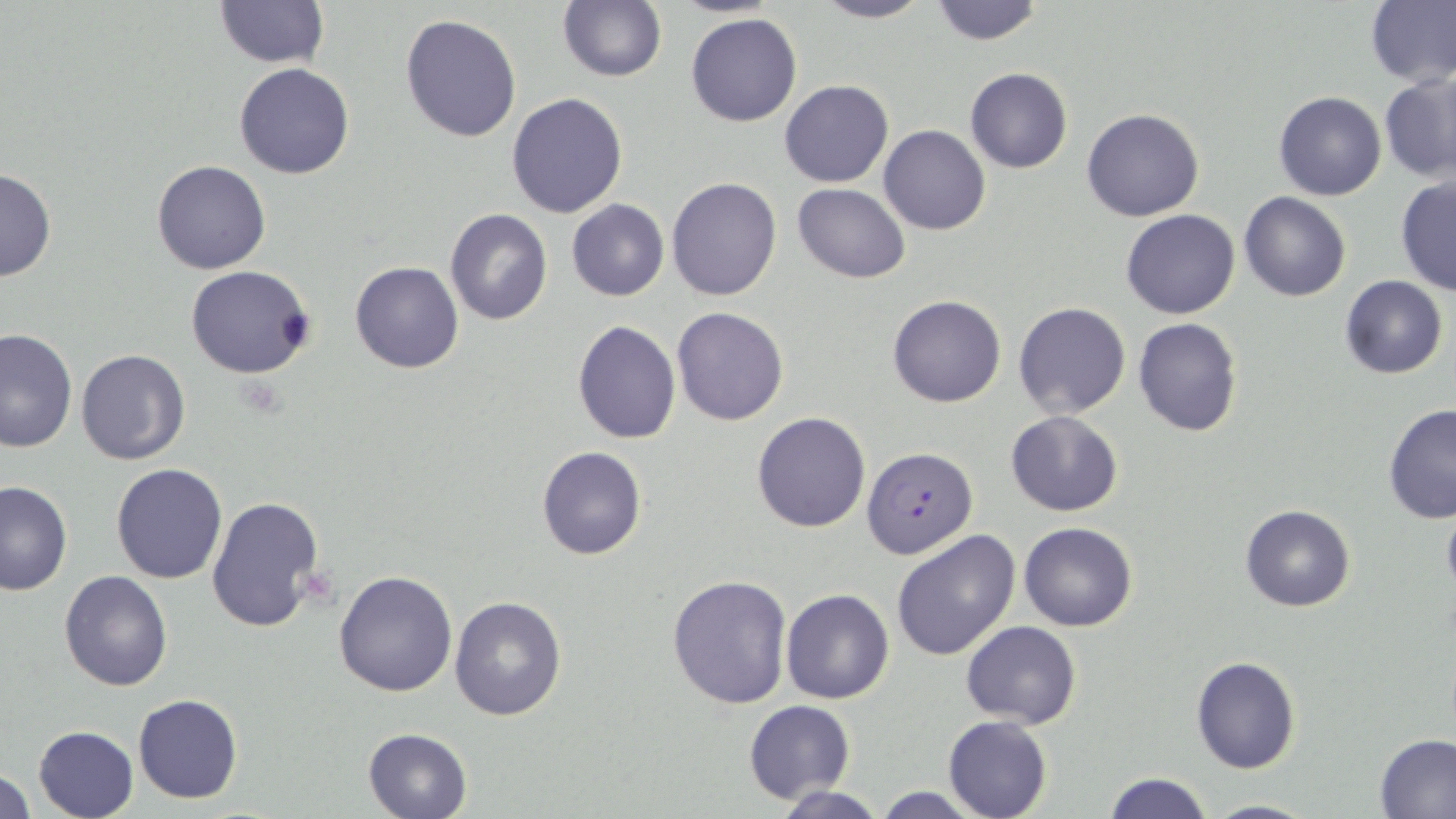
Summary:
  - Coordinate format: approximate bounding boxes as (x1, y1, x2, y2) in pixels
  - Plasmodium falciparum-infected red blood cell locations: (867, 447, 982, 559)
  - Uninfected red blood cell locations: (213, 0, 328, 68), (557, 0, 667, 82), (808, 0, 935, 24), (928, 0, 1045, 46), (1366, 0, 1456, 88), (685, 12, 803, 126), (401, 14, 521, 142), (235, 63, 355, 180), (965, 68, 1072, 174), (1380, 74, 1456, 182), (779, 80, 893, 188), (1273, 91, 1387, 202), (507, 92, 628, 218), (1082, 107, 1203, 221), (879, 125, 991, 235), (151, 159, 270, 274), (0, 166, 57, 283), (667, 176, 781, 301), (1395, 176, 1456, 297), (792, 182, 910, 283), (1239, 191, 1351, 302), (567, 200, 669, 302), (445, 209, 553, 327), (1120, 209, 1240, 319), (350, 261, 463, 374), (186, 265, 316, 379), (1339, 275, 1448, 379), (887, 295, 1006, 407), (1012, 302, 1131, 419), (671, 306, 790, 426), (1133, 317, 1242, 438), (572, 319, 680, 443), (0, 328, 78, 453), (76, 348, 190, 465), (1382, 402, 1456, 524), (1004, 410, 1123, 516), (751, 412, 870, 532), (536, 446, 647, 560), (111, 463, 227, 584), (0, 481, 73, 596), (207, 495, 326, 632), (1441, 498, 1456, 602), (1239, 504, 1354, 613), (1019, 522, 1137, 631), (892, 530, 1022, 662), (333, 571, 458, 696), (59, 572, 173, 692), (667, 572, 793, 709), (781, 589, 894, 704), (448, 596, 567, 722), (961, 621, 1081, 730), (1191, 656, 1300, 773), (133, 693, 243, 804), (743, 700, 855, 803), (943, 716, 1051, 819), (33, 724, 139, 818), (363, 727, 473, 818), (1375, 735, 1456, 817), (1, 769, 34, 819), (1104, 773, 1214, 819), (770, 785, 887, 819), (869, 787, 986, 818), (1204, 796, 1317, 818)
  - Slide-level diagnosis: Plasmodium falciparum
  - Field of view: single
  - Preparation: thin blood film
  - Modality: light microscopy
  - Magnification: 1000x
  - Stain: May-Grünwald-Giemsa
  - Image size: 1456×819 pixels